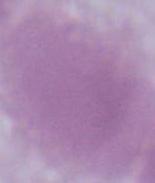 An erythrocyte is seen. Micrograph. Captured at 1000x magnification.